Name the parasite shown.
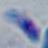
This is Toxoplasma gondii.

{
  "magnification": "1000x",
  "modality": "photomicrograph"
}